Identify the blood parasite species.
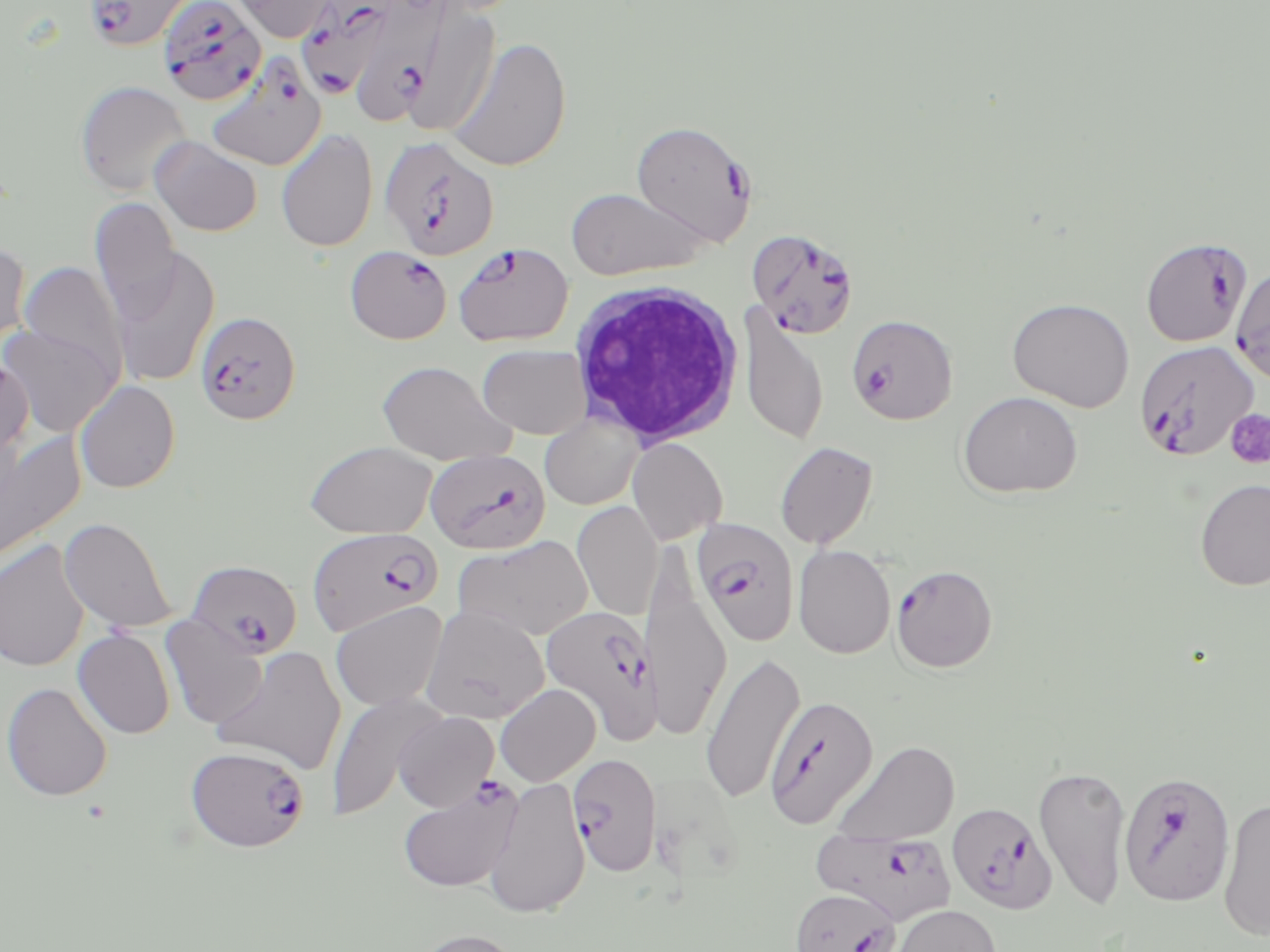
Plasmodium falciparum.

Approximate bounding boxes as (x1,y1)-(x2,y2) corner pairs in pixels. Platelet locations: (1225,409)-(1270,470). White blood cell locations: (567,281)-(746,449). Plasmodium falciparum-infected red blood cell locations (subset): (82,0)-(197,52), (358,0)-(450,119), (157,1)-(268,106), (294,1)-(403,100), (208,56)-(329,171), (631,120)-(757,246), (379,136)-(500,261), (746,229)-(860,339), (1140,237)-(1252,347), (452,242)-(574,347), (345,245)-(453,344), (195,310)-(301,425), (847,314)-(958,424), (1133,340)-(1260,462), (425,448)-(550,554), (692,518)-(800,647), (308,527)-(442,637), (187,559)-(301,658), (890,564)-(998,673), (540,605)-(662,743), (186,744)-(309,853), (568,753)-(662,877), (397,776)-(523,893), (947,802)-(1057,913), (812,828)-(957,926), (790,888)-(900,952). Uninfected red blood cell locations (subset): (230,0)-(338,42), (418,3)-(501,146), (447,37)-(571,171), (75,80)-(192,197), (276,128)-(378,252), (150,136)-(263,237), (565,187)-(708,280), (90,197)-(182,322), (0,242)-(31,355), (110,246)-(221,387), (19,261)-(128,381), (1231,264)-(1270,383), (1007,297)-(1135,412), (739,304)-(828,446), (0,323)-(119,436), (477,344)-(592,440), (0,358)-(33,462), (376,360)-(514,465), (75,380)-(180,493), (957,391)-(1082,498), (539,412)-(644,510), (0,428)-(85,569), (627,438)-(727,544), (304,441)-(437,539), (775,441)-(879,549), (1195,479)-(1270,591), (573,500)-(663,621), (59,517)-(177,633), (453,534)-(593,641), (0,539)-(90,672), (793,544)-(896,659), (642,571)-(731,742), (330,601)-(447,712), (421,604)-(550,724), (161,613)-(268,730), (73,628)-(175,739), (212,645)-(346,774), (700,651)-(805,805), (1,682)-(113,801), (495,684)-(600,786), (326,691)-(445,820), (394,711)-(499,812), (833,740)-(960,846), (1034,763)-(1133,912), (484,776)-(591,918), (1218,797)-(1270,942), (891,904)-(1002,952), (409,928)-(526,952). One field of a larger specimen. Light microscopy. Thin blood smear. Captured at 1000x magnification. May-Grünwald-Giemsa-stained preparation. Image is 1270×952 pixels.